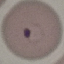
Summary:
  - Malaria status: parasitized
  - Preparation: thin blood film
  - Capture: smartphone through the microscope eyepiece
  - Image type: cell patch, automatically extracted from a larger field of view and resized to 64 × 64 pixels
  - Stain: Giemsa